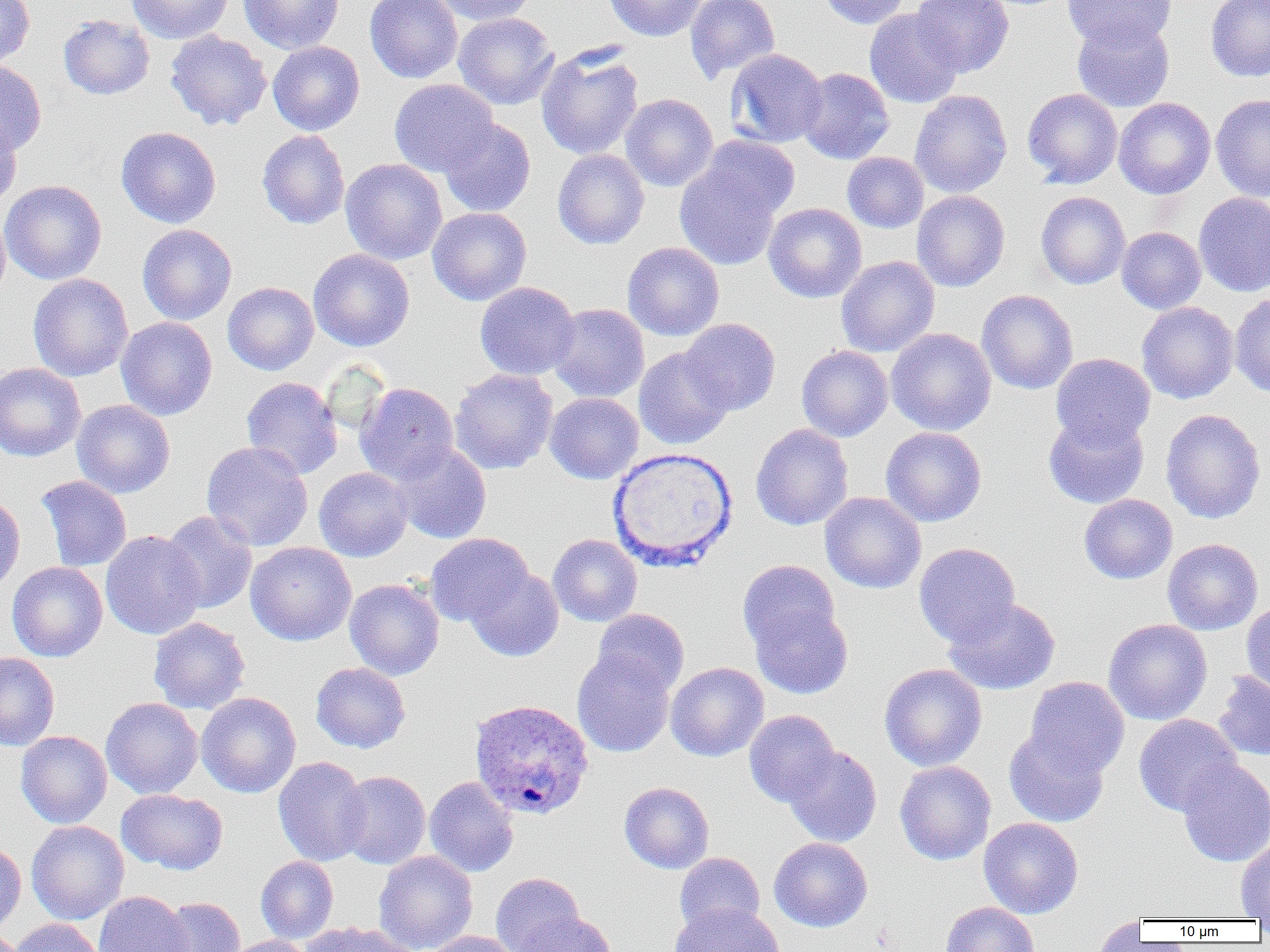
Summary:
  - Coordinate format: approximate bounding boxes as [x1, y1, x2, y2] in pixels
  - Uninfected red blood cell locations: [0, 0, 35, 68], [126, 0, 234, 44], [238, 0, 345, 54], [365, 0, 463, 83], [432, 0, 536, 26], [604, 0, 707, 42], [684, 0, 780, 83], [818, 0, 911, 28], [911, 0, 1014, 78], [1063, 0, 1176, 52], [1205, 0, 1270, 82], [864, 8, 964, 109], [453, 12, 559, 110], [58, 14, 155, 100], [1071, 17, 1175, 112], [164, 29, 272, 131], [267, 41, 365, 136], [536, 45, 644, 161], [725, 48, 827, 148], [0, 60, 46, 156], [796, 67, 894, 164], [389, 78, 498, 178], [1022, 88, 1123, 188], [910, 89, 1012, 198], [620, 93, 718, 192], [1210, 93, 1270, 202], [1113, 98, 1215, 199], [0, 114, 23, 211], [439, 118, 536, 217], [116, 126, 221, 228], [257, 129, 350, 229], [698, 134, 801, 222], [552, 149, 650, 250], [842, 152, 929, 233], [340, 158, 447, 264], [674, 161, 782, 270], [1, 180, 107, 285], [911, 190, 1010, 292], [1036, 191, 1130, 289], [1194, 191, 1270, 297], [764, 203, 866, 303], [427, 207, 531, 306], [0, 208, 11, 306], [137, 224, 237, 325], [1116, 226, 1206, 314], [622, 241, 724, 341], [308, 249, 415, 352], [836, 255, 939, 357], [27, 273, 133, 381], [222, 281, 319, 375], [475, 281, 580, 380], [976, 289, 1078, 394], [1229, 292, 1270, 399], [1136, 301, 1238, 404], [548, 303, 649, 403], [116, 317, 217, 420], [679, 318, 781, 415], [886, 328, 997, 435], [796, 345, 893, 442], [634, 346, 734, 450], [1050, 353, 1156, 449], [0, 362, 86, 462], [450, 369, 558, 474], [241, 376, 343, 479], [355, 382, 459, 484], [545, 392, 643, 484], [71, 399, 175, 498], [1160, 408, 1266, 524], [1043, 413, 1149, 509], [750, 423, 853, 530], [880, 426, 987, 527], [201, 441, 313, 551], [391, 442, 491, 544], [314, 467, 412, 562], [36, 475, 132, 572], [819, 492, 926, 594], [0, 494, 25, 595], [1079, 494, 1177, 584], [160, 510, 257, 614], [100, 530, 205, 640], [425, 533, 534, 627], [548, 534, 643, 627], [1162, 538, 1263, 635], [245, 542, 356, 646], [914, 542, 1020, 647], [737, 559, 841, 658], [7, 561, 107, 662], [465, 567, 564, 662], [344, 578, 444, 680], [942, 597, 1061, 695], [748, 598, 854, 699], [1241, 601, 1270, 698], [592, 608, 689, 697], [148, 617, 250, 715], [1103, 618, 1212, 725], [572, 649, 676, 757], [0, 653, 60, 751], [310, 662, 411, 753], [665, 662, 769, 762], [879, 663, 987, 771], [1213, 671, 1270, 761], [1024, 676, 1129, 777], [196, 692, 301, 798], [101, 697, 203, 799], [744, 709, 839, 807], [1133, 714, 1242, 817], [1004, 727, 1109, 827], [15, 731, 112, 828], [783, 745, 882, 847], [273, 756, 371, 867], [1177, 758, 1270, 867], [894, 760, 996, 865], [337, 770, 431, 869], [424, 776, 519, 877], [619, 782, 714, 874], [116, 788, 228, 874], [978, 817, 1083, 918], [26, 820, 129, 924], [769, 837, 873, 932], [1235, 838, 1270, 920], [0, 842, 26, 935], [374, 851, 478, 952], [674, 852, 766, 937], [256, 856, 339, 943], [491, 872, 584, 952], [93, 891, 193, 952], [156, 897, 246, 952], [940, 901, 1039, 952], [670, 902, 783, 952], [515, 911, 616, 952], [1088, 917, 1148, 951], [8, 918, 105, 952], [299, 921, 415, 952], [425, 930, 520, 952], [223, 935, 314, 952]
  - Plasmodium ovale-infected red blood cell locations: [469, 698, 595, 819]
  - White blood cell locations: [608, 446, 738, 571]
  - Slide-level diagnosis: Plasmodium ovale
  - Modality: light microscopy
  - Preparation: thin blood smear
  - Field of view: single
  - Magnification: 1000x
  - Image size: 1270×952 pixels